State the preparation type.
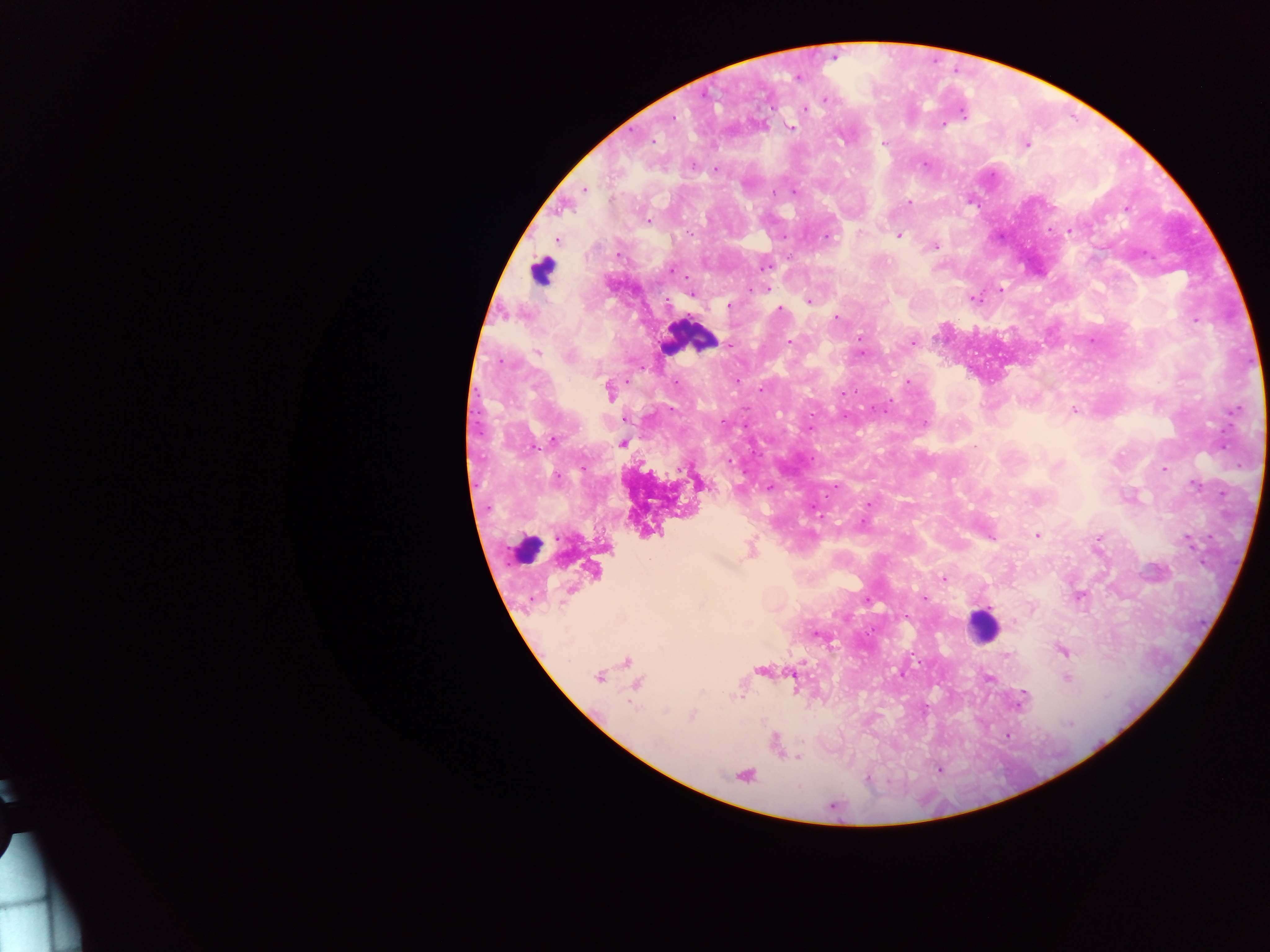
This is a thick smear.

field of view = single
capture = mobile-phone photograph through a microscope
Plasmodium parasite locations = approximate centers as (x, y) in pixels: (833, 58), (797, 77), (824, 100), (804, 108), (961, 111), (674, 119), (942, 124), (790, 128), (630, 129), (654, 143), (884, 143), (1026, 144), (924, 166), (715, 169), (992, 172), (585, 189), (793, 192), (773, 193), (970, 199), (908, 201), (1126, 209), (647, 219), (1048, 229), (1068, 231), (826, 235), (783, 236), (899, 236), (1000, 237), (556, 239), (933, 246), (1144, 251), (763, 266), (671, 269), (766, 288), (999, 290), (691, 293), (972, 297), (808, 301), (729, 305), (780, 308), (836, 319), (1194, 320), (1092, 338), (790, 342), (912, 343), (730, 344), (537, 352), (863, 354), (569, 356), (1251, 363), (502, 365), (907, 382), (473, 390), (760, 390), (610, 392), (844, 392), (890, 400), (1238, 408), (1074, 409), (478, 411), (886, 412), (844, 418), (724, 419), (745, 423), (923, 423), (811, 427), (1221, 432), (482, 433), (553, 439), (622, 443), (532, 449), (1221, 450), (810, 457), (728, 460), (583, 469), (1163, 469), (742, 470), (559, 476), (1188, 480), (768, 486), (474, 487), (836, 488), (1217, 492), (826, 498), (869, 503), (812, 504), (487, 507), (860, 521), (1036, 534), (557, 535), (988, 535), (1188, 539), (750, 550), (1202, 560), (593, 571), (943, 579), (1078, 596), (924, 597), (865, 599), (1204, 623), (815, 633), (1062, 650), (911, 655), (1004, 657), (626, 662), (761, 670), (900, 674), (598, 675), (987, 677), (1066, 677), (636, 683), (1022, 698), (691, 715), (1007, 735), (775, 742), (796, 757), (938, 769), (743, 774), (868, 777)
country = Ghana
leukocyte locations = approximate centers as (x, y) in pixels: (541, 270), (689, 337), (526, 550), (982, 625)
image size = 1270×952 pixels